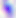

magnification: 400x
modality: photomicrograph
identification: Toxoplasma gondii